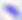

Summary:
  - Modality: photomicrograph
  - Identification: Toxoplasma gondii
  - Magnification: 400x